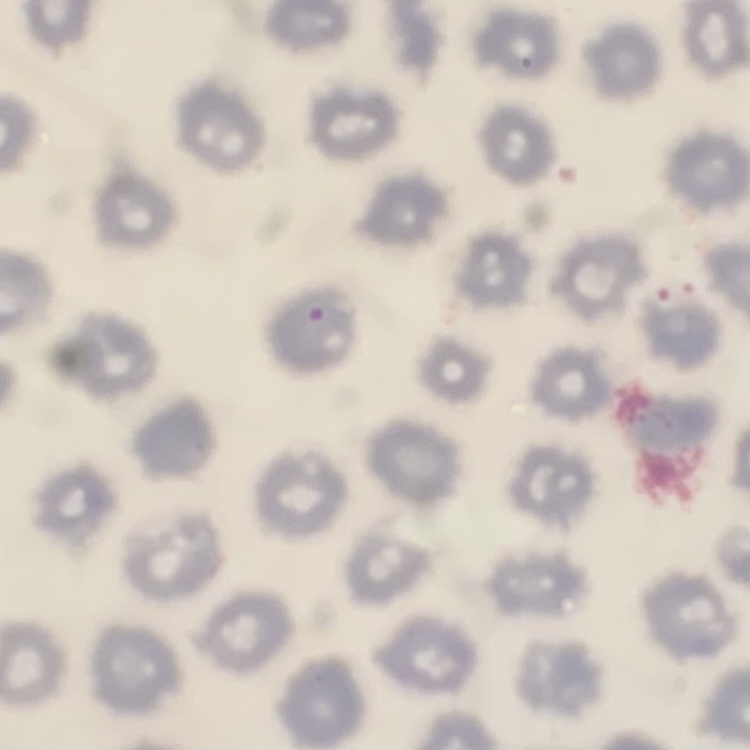
The red blood cells show no rouleaux formation. Stained with either Field's or Giemsa. Square crop of a larger photomicrograph. Thin blood film.